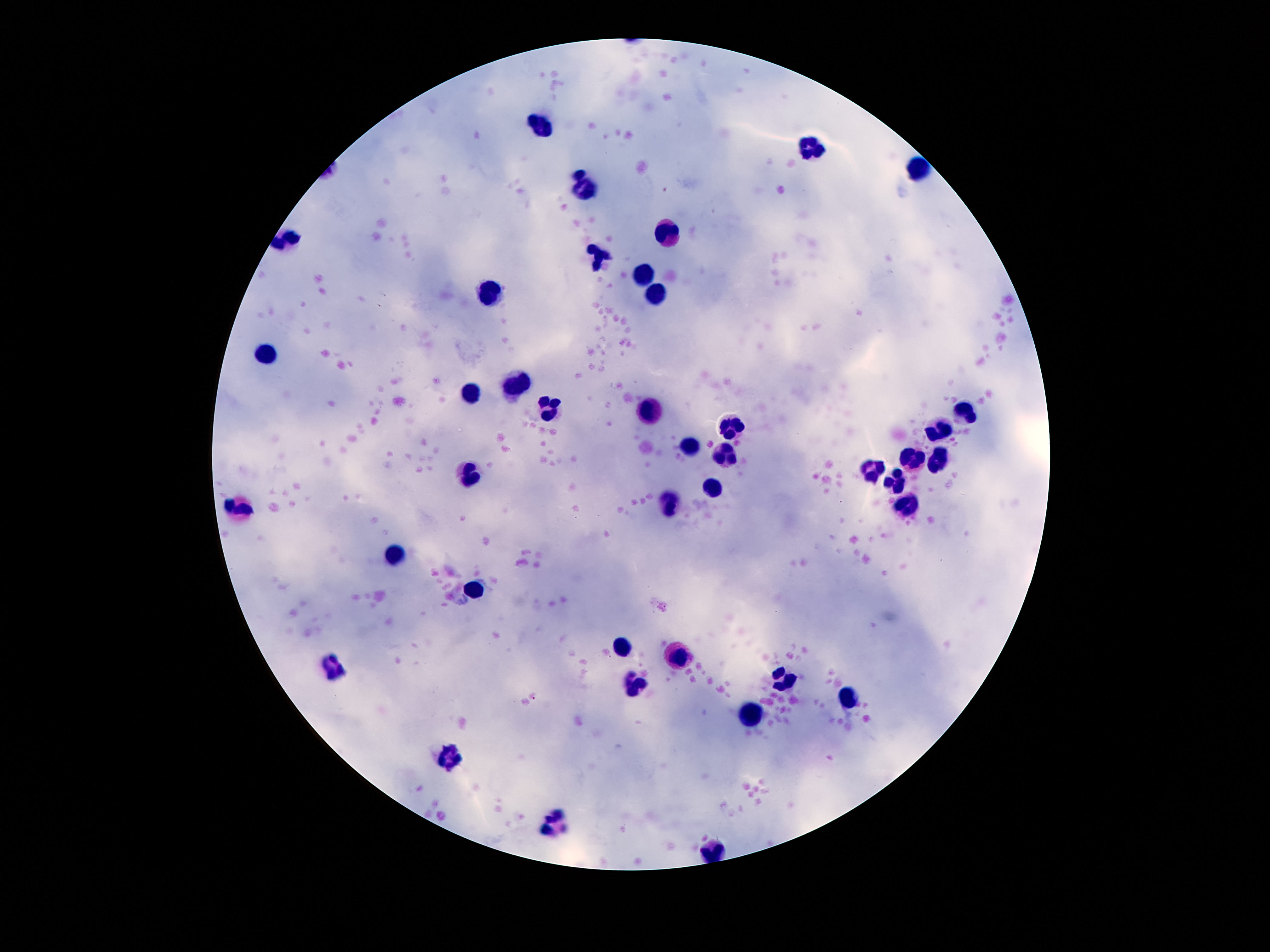

magnification: 100x
capture: smartphone camera through the microscope eyepiece
image_size: 1270×952 pixels
preparation: thick blood smear
stain: Giemsa
leukocyte_locations: 'approximate centers as (x, y) in pixels: (536, 127), (808, 148), (919, 168), (585, 191), (667, 235), (599, 258), (644, 275), (658, 293), (490, 297), (265, 352), (515, 387), (470, 392), (651, 407), (549, 409), (964, 414), (731, 428), (939, 434), (690, 445), (724, 454), (912, 459), (940, 459), (470, 472), (871, 472), (896, 486), (713, 491), (670, 505), (906, 506), (236, 509), (391, 552), (472, 588), (622, 647), (679, 658), (331, 666), (783, 681), (638, 687), (849, 699), (747, 714), (449, 758), (558, 820)'
field_of_view: one from this slide
patient_malaria_status: uninfected